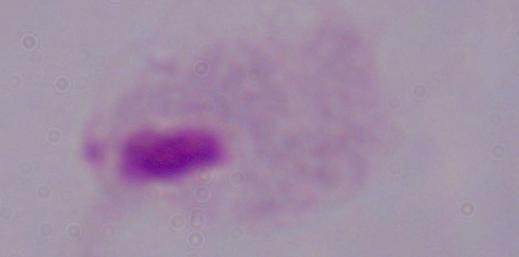

Summary:
  - Identification: trichomonad
  - Modality: micrograph
  - Magnification: 1000x